Locate every blood parasite and identify its species.
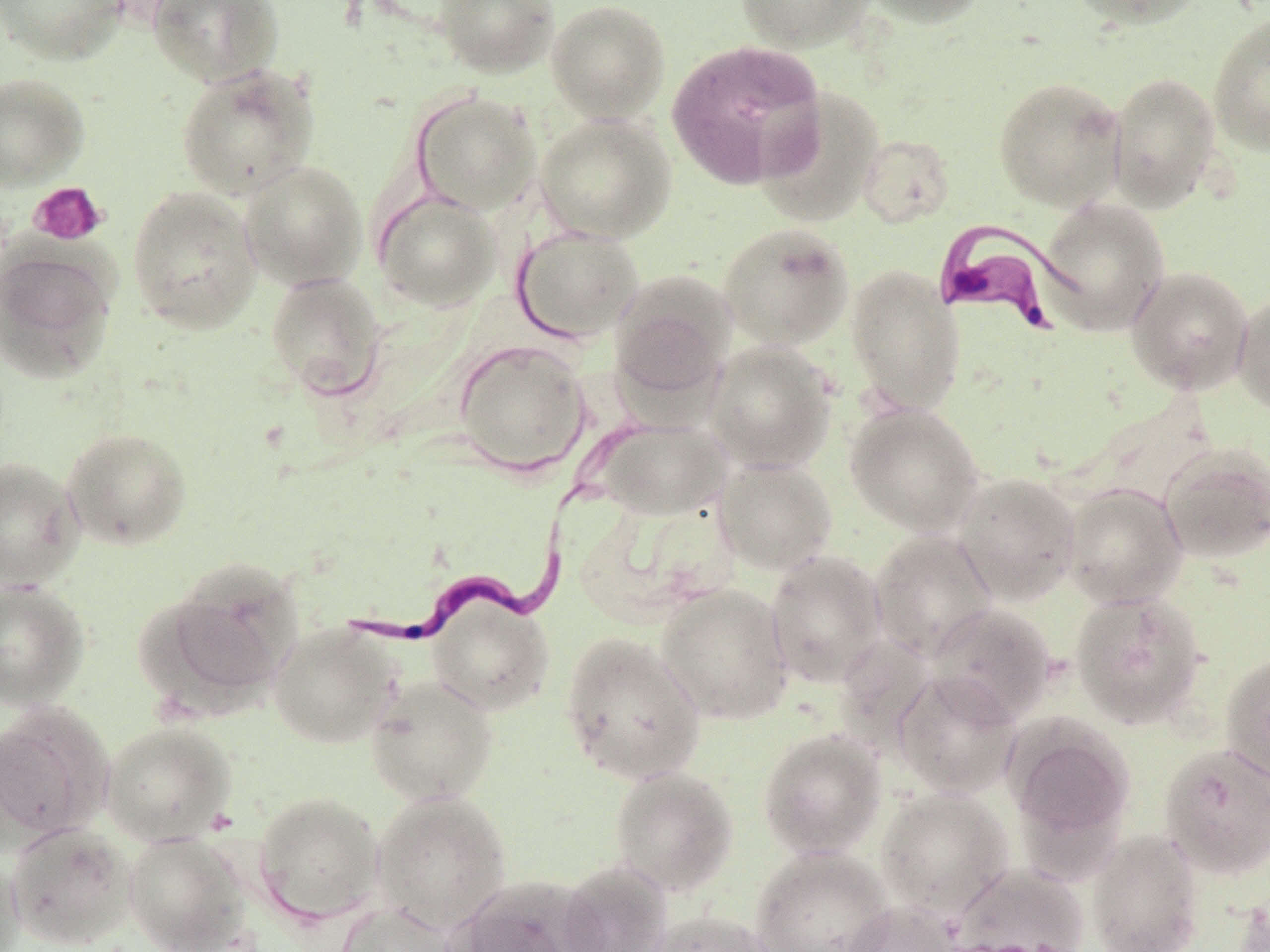
Approximate bounding boxes as [x1, y1, x2, y2] in pixels.
Trypanosoma brucei: [932, 218, 1077, 333], [329, 478, 576, 652].
No Plasmodium falciparum, Plasmodium ovale, Plasmodium malariae, Plasmodium vivax, or Babesia divergens observed.

{
  "slide_level_diagnosis": "Trypanosoma brucei",
  "stain": "May-Grünwald-Giemsa",
  "preparation": "thin blood film",
  "modality": "optical microscopy",
  "field_of_view": "single",
  "platelet_locations": "approximate bounding boxes as [x1, y1, x2, y2] in pixels: [28, 181, 108, 247]",
  "image_size": "1270×952 pixels",
  "magnification": "1000x",
  "uninfected_red_blood_cell_locations": "approximate bounding boxes as [x1, y1, x2, y2] in pixels: [0, 0, 127, 65], [433, 0, 559, 78], [545, 0, 671, 124], [736, 0, 874, 53], [861, 0, 988, 28], [1068, 0, 1209, 31], [147, 1, 283, 87], [1208, 13, 1270, 157], [666, 39, 827, 189], [175, 63, 320, 199], [1107, 70, 1222, 212], [0, 73, 90, 191], [993, 76, 1126, 211], [754, 87, 886, 227], [411, 90, 542, 216], [535, 112, 677, 243], [857, 134, 955, 228], [239, 160, 368, 291], [128, 186, 262, 333], [373, 189, 502, 311], [1036, 197, 1169, 335], [717, 222, 854, 350], [512, 225, 644, 344], [0, 244, 117, 382], [845, 265, 966, 416], [1126, 265, 1254, 394], [610, 269, 738, 402], [265, 272, 387, 399], [1233, 292, 1270, 416], [453, 339, 591, 476], [704, 341, 837, 474], [845, 401, 985, 537], [591, 416, 733, 520], [62, 427, 192, 551], [1158, 441, 1270, 565], [714, 456, 838, 575], [0, 458, 84, 589], [953, 472, 1082, 605], [1062, 483, 1187, 608], [869, 530, 998, 661], [765, 550, 888, 688], [145, 559, 304, 714], [0, 579, 90, 710], [655, 583, 794, 724], [1070, 589, 1207, 729], [427, 596, 555, 715], [925, 602, 1058, 726], [268, 622, 402, 748], [560, 632, 706, 785], [1219, 651, 1270, 784], [891, 669, 1022, 799], [365, 675, 498, 807], [0, 705, 113, 841], [1006, 719, 1134, 845], [101, 720, 236, 844], [757, 728, 888, 861], [1159, 743, 1270, 879], [609, 765, 739, 896], [876, 787, 1014, 918], [371, 789, 512, 934], [253, 791, 385, 924], [6, 821, 137, 949], [1086, 829, 1205, 952], [123, 832, 252, 952], [751, 845, 894, 952], [0, 852, 25, 952], [557, 860, 673, 952], [950, 864, 1090, 952], [448, 875, 602, 952], [1233, 889, 1270, 952], [843, 901, 964, 952], [335, 902, 461, 952], [645, 910, 780, 952]"
}